Assess the morphology of the red blood cells.
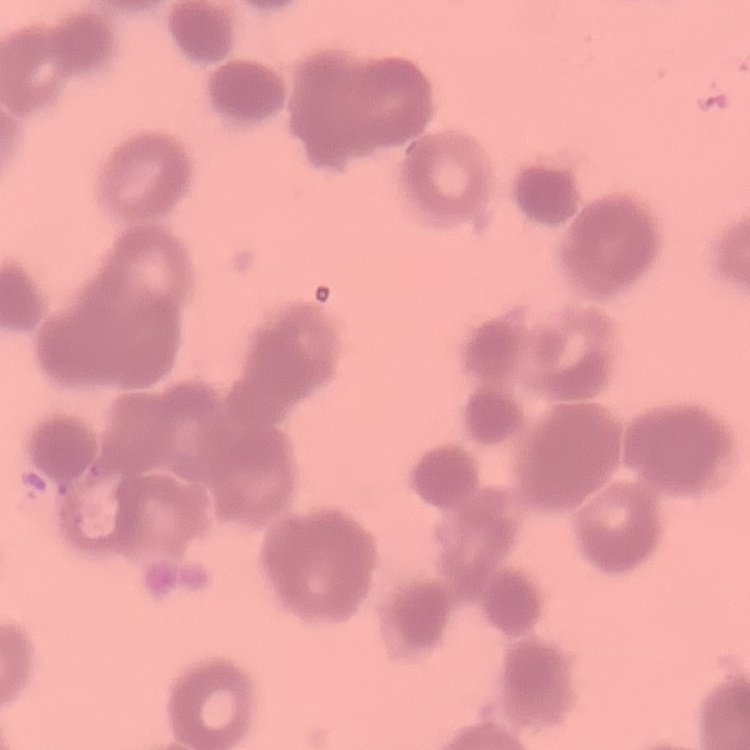

They show rouleaux formation.

Summary:
  - Preparation: thin blood film
  - Image type: square crop of a larger photomicrograph
  - Stain: Field's or Giemsa